State which parasite is depicted.
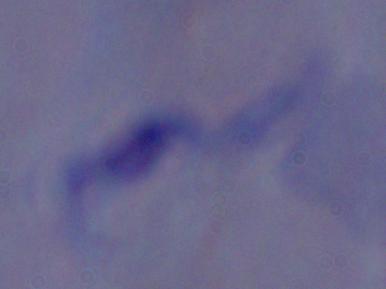

A trypanosome.

Photomicrograph. Captured at 1000x magnification.